Comment on the morphology of the red blood cells.
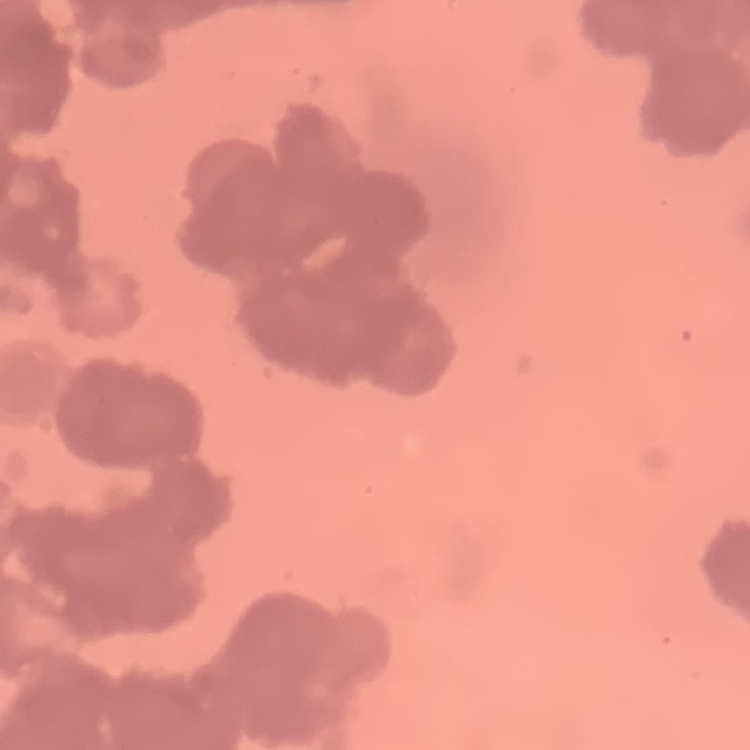
Rouleaux formation.

stain = Field's or Giemsa
preparation = thin peripheral smear
image type = square crop of a larger photomicrograph